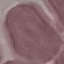
Summary:
  - Result: no malaria parasites detected
  - Preparation: thin smear
  - Stain: Giemsa
  - Image type: cell patch, automatically extracted from a larger field of view and resized to 64 × 64 pixels
  - Capture: smartphone through the microscope eyepiece